Name the cell type shown.
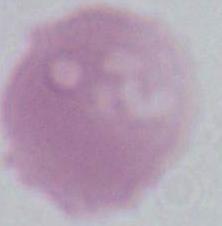
This is an erythrocyte.

1000x magnification. Micrograph.